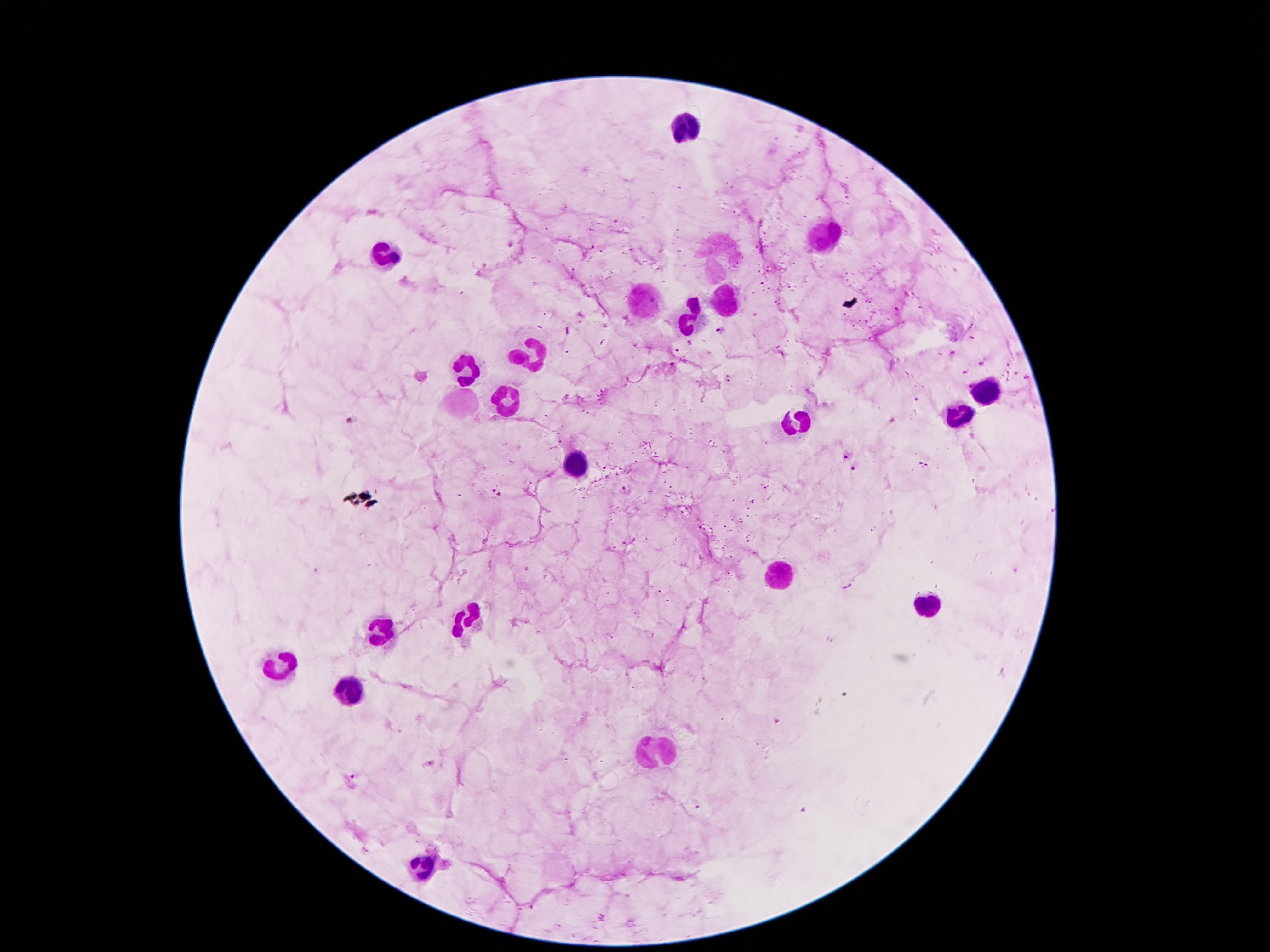

Approximate centers as (x, y) in pixels.
Summary:
  - Leukocyte locations: (686, 128), (820, 240), (721, 256), (384, 258), (648, 299), (727, 303), (689, 319), (533, 357), (465, 370), (984, 390), (506, 400), (457, 408), (960, 414), (793, 424), (579, 461), (779, 575), (926, 608), (465, 620), (383, 632), (279, 663), (352, 689), (658, 749), (422, 864)
  - Plasmodium parasite locations: (511, 244), (720, 328), (689, 342), (952, 353), (728, 378), (1027, 379), (350, 420), (846, 455), (853, 467), (625, 489), (494, 491)
  - Patient malaria status: infected with Plasmodium falciparum
  - Stain: Giemsa
  - Image size: 1270×952 pixels
  - Field of view: one from this slide
  - Magnification: 100x
  - Capture: smartphone camera through the microscope eyepiece
  - Preparation: thick peripheral-blood smear